State which parasite is depicted.
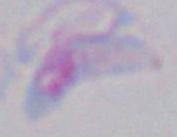
This is Toxoplasma gondii.

Summary:
  - Magnification: 1000x
  - Modality: photomicrograph